Assess this cell for malaria.
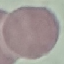
It is uninfected.

Thin blood film. Giemsa stain. Acquired by smartphone through the microscope eyepiece. Cell patch, automatically extracted from a larger field of view and resized to 64 × 64 pixels.